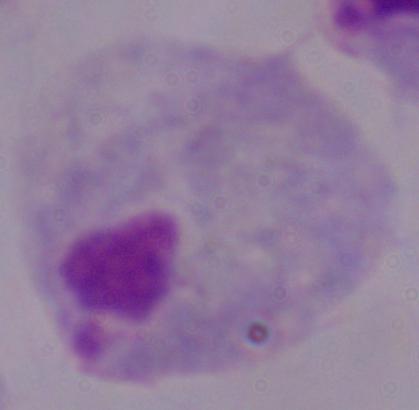
{
  "identification": "trichomonad",
  "magnification": "1000x",
  "modality": "micrograph"
}